Name the parasite shown.
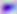

Toxoplasma gondii.

magnification: 400x
modality: micrograph